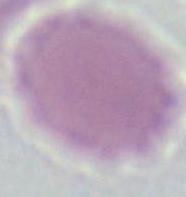

{
  "modality": "photomicrograph",
  "identification": "erythrocyte",
  "magnification": "1000x"
}